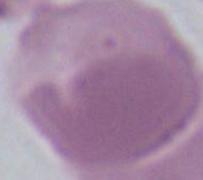

magnification = 1000x
modality = micrograph
identification = red blood cell